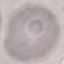 Result: negative for malaria parasites. Cell patch, automatically extracted from a larger field of view and resized to 64 × 64 pixels. Giemsa-stained preparation. Thin smear of blood. Photographed with a smartphone camera at the microscope eyepiece.